Report the malaria status of this cell.
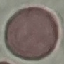

Uninfected.

Cell patch, automatically extracted from a larger field of view and resized to 64 × 64 pixels. Giemsa-stained preparation. Acquired by smartphone through the microscope eyepiece. Thin blood film.